Locate and identify every blood parasite.
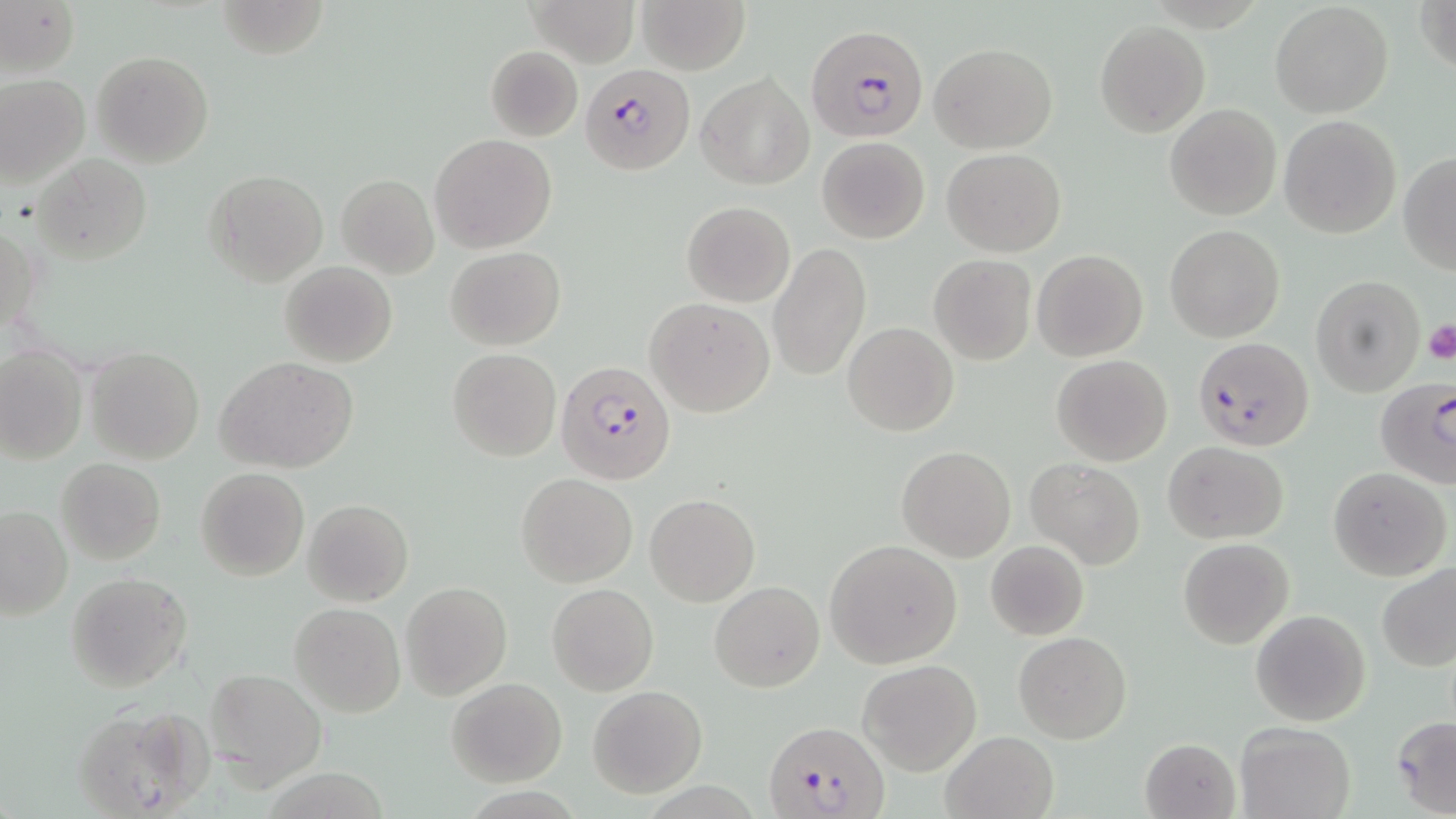

Approximate bounding boxes as [x1, y1, x2, y2] in pixels.
Plasmodium falciparum-infected red blood cells: [806, 24, 930, 144], [581, 63, 694, 175], [1192, 337, 1313, 449], [555, 359, 678, 485], [1375, 376, 1454, 488], [763, 717, 890, 819].
No Plasmodium ovale, Plasmodium malariae, Plasmodium vivax, Babesia divergens, or Trypanosoma brucei observed.

Summary:
  - Platelet locations: [1421, 319, 1456, 364]
  - Uninfected red blood cell locations: [210, 0, 326, 60], [527, 0, 639, 67], [635, 0, 752, 73], [1415, 0, 1456, 80], [1, 2, 80, 78], [1269, 2, 1394, 119], [1095, 21, 1209, 136], [930, 43, 1056, 151], [484, 46, 583, 142], [91, 50, 214, 167], [696, 72, 813, 189], [0, 74, 89, 187], [1165, 104, 1281, 220], [1279, 115, 1402, 239], [431, 134, 556, 252], [816, 136, 930, 242], [943, 148, 1066, 257], [1398, 153, 1456, 273], [34, 155, 150, 265], [204, 169, 327, 286], [336, 175, 438, 278], [682, 200, 795, 306], [1, 217, 41, 341], [1165, 224, 1285, 343], [768, 242, 872, 382], [445, 247, 565, 349], [1032, 248, 1148, 362], [929, 255, 1037, 366], [280, 261, 397, 367], [1311, 275, 1426, 396], [645, 297, 771, 417], [843, 322, 958, 436], [0, 346, 86, 464], [85, 347, 205, 465], [447, 348, 561, 461], [1051, 354, 1173, 465], [216, 355, 359, 474], [1164, 440, 1288, 544], [897, 446, 1015, 562], [56, 457, 166, 567], [1024, 457, 1146, 569], [196, 467, 308, 580], [1328, 467, 1451, 582], [516, 473, 637, 586], [645, 493, 758, 605], [302, 497, 414, 606], [0, 506, 73, 620], [826, 539, 963, 667], [1179, 539, 1294, 647], [985, 541, 1089, 639], [1375, 562, 1455, 673], [66, 572, 191, 692], [710, 581, 824, 693], [400, 582, 512, 700], [547, 583, 659, 696], [288, 603, 406, 718], [1250, 608, 1372, 727], [1014, 631, 1131, 744], [857, 658, 982, 774], [205, 667, 326, 790], [445, 678, 567, 787], [589, 685, 707, 798], [71, 704, 212, 819], [1391, 716, 1456, 816], [1235, 721, 1355, 819], [941, 729, 1058, 819], [1141, 737, 1241, 818]
  - Slide-level diagnosis: Plasmodium falciparum
  - Preparation: thin blood smear
  - Modality: light microscopy
  - Field of view: single
  - Stain: May-Grünwald-Giemsa
  - Magnification: 1000x
  - Image size: 1456×819 pixels